Identify the preparation type.
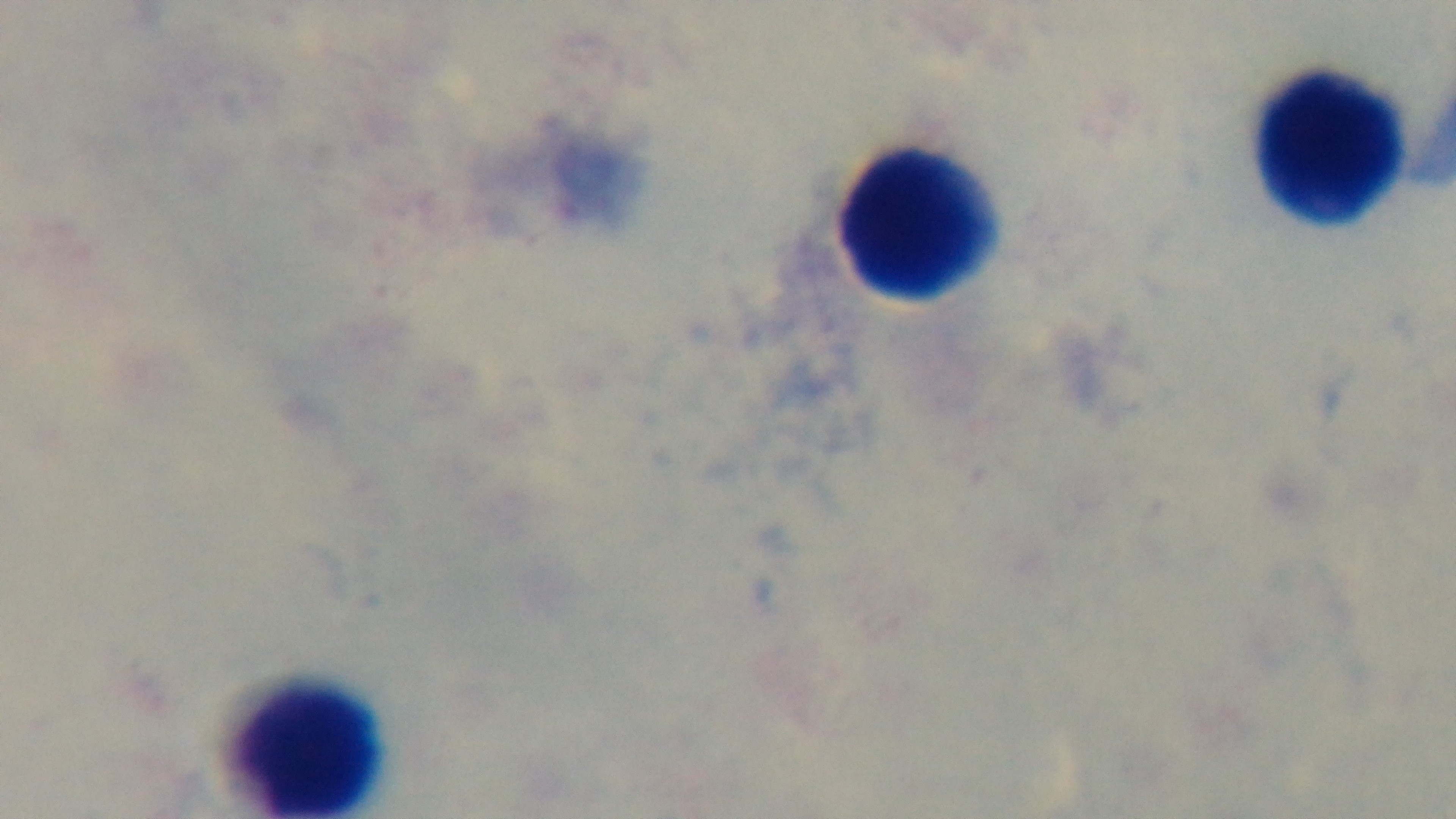

A thick smear.

{
  "objective": "100x oil immersion",
  "malaria_status": "negative",
  "capture": "mounted 4K digital camera",
  "modality": "light microscopy",
  "field_of_view": "one from the slide",
  "stain": "Giemsa"
}